Assess this cell for malaria.
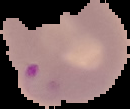

It is parasitized.

Summary:
  - Image size: 130×109 pixels
  - Image type: segmented cell region on a black background
  - Preparation: thin blood film